Report the malaria status of this cell.
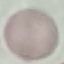

It is uninfected.

image type = cell patch, automatically extracted from a larger field of view and resized to 64 × 64 pixels
preparation = thin blood smear
capture = smartphone camera at the microscope eyepiece
stain = Giemsa